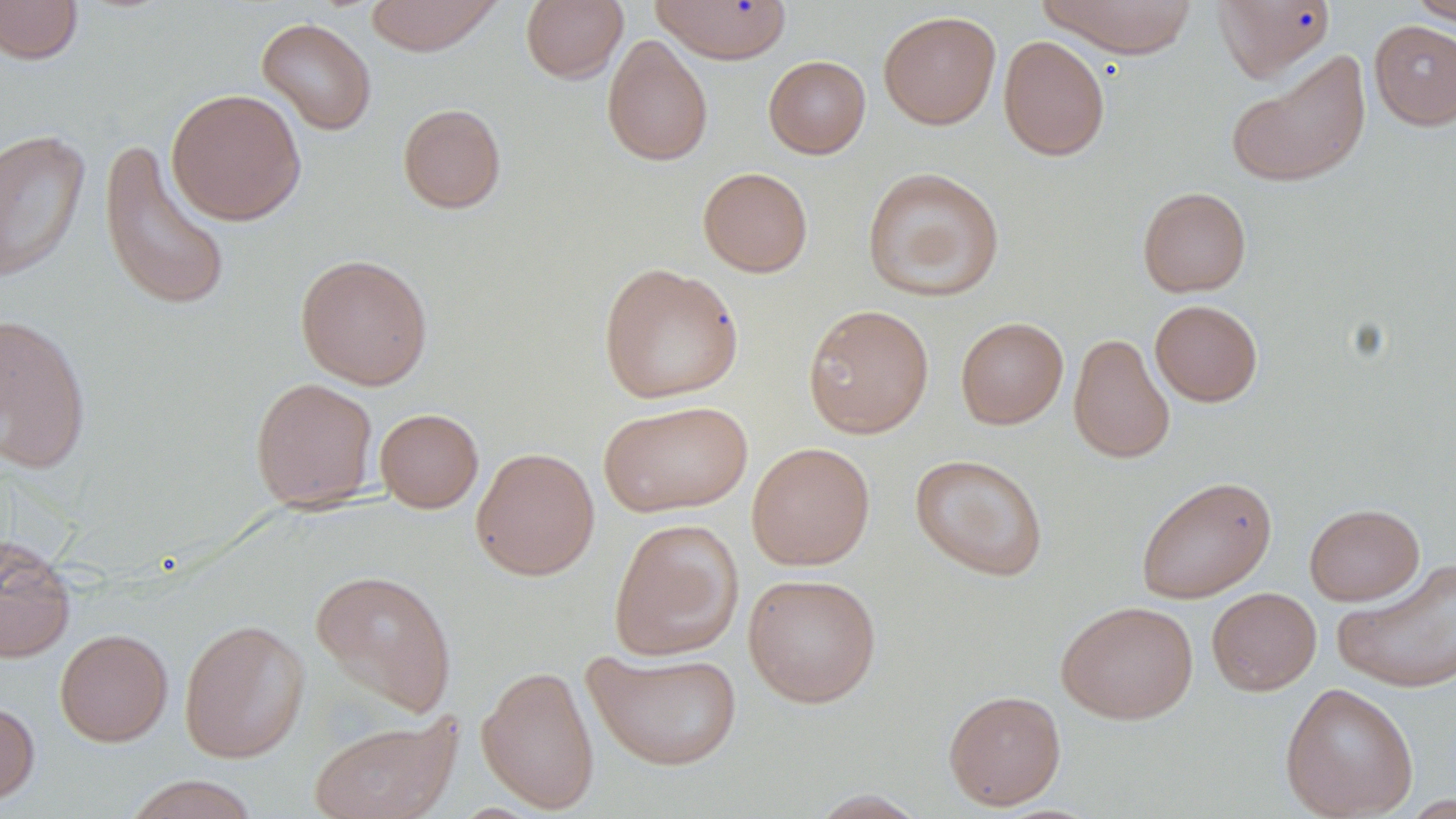

Summary:
  - Coordinate format: approximate bounding boxes as [x1, y1, x2, y2] in pixels
  - Uninfected red blood cell locations: [365, 0, 503, 56], [520, 0, 628, 84], [1037, 0, 1199, 59], [1211, 0, 1336, 83], [1406, 0, 1456, 26], [0, 1, 84, 65], [650, 1, 792, 63], [878, 10, 1001, 129], [257, 17, 377, 136], [1369, 20, 1456, 130], [602, 34, 714, 167], [997, 35, 1110, 161], [1225, 50, 1372, 189], [763, 55, 871, 158], [166, 88, 307, 226], [397, 103, 507, 214], [0, 128, 91, 283], [98, 138, 231, 314], [862, 166, 1005, 302], [698, 167, 813, 277], [1137, 187, 1251, 297], [294, 253, 434, 390], [598, 262, 744, 404], [1150, 299, 1263, 406], [802, 304, 934, 438], [0, 313, 92, 473], [955, 316, 1069, 429], [1068, 333, 1175, 464], [250, 377, 379, 511], [598, 399, 754, 518], [375, 407, 484, 513], [746, 441, 876, 570], [471, 446, 600, 580], [910, 453, 1049, 581], [1135, 475, 1277, 603], [1304, 503, 1424, 605], [608, 518, 745, 661], [0, 535, 76, 663], [1332, 558, 1455, 693], [310, 569, 457, 717], [743, 573, 882, 708], [1207, 587, 1321, 696], [1056, 600, 1199, 724], [178, 618, 310, 763], [55, 628, 172, 746], [583, 648, 743, 771], [476, 664, 600, 813], [1279, 681, 1418, 819], [943, 689, 1067, 810], [0, 699, 39, 806], [308, 714, 462, 819], [123, 775, 261, 818], [807, 790, 930, 818]
  - Slide-level diagnosis: negative for blood parasites
  - Field of view: single
  - Modality: optical microscopy
  - Stain: May-Grünwald-Giemsa
  - Image size: 1456×819 pixels
  - Preparation: thin blood smear
  - Magnification: 1000x